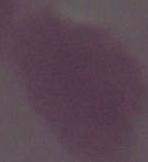 1000x magnification. An erythrocyte is seen. Photomicrograph.